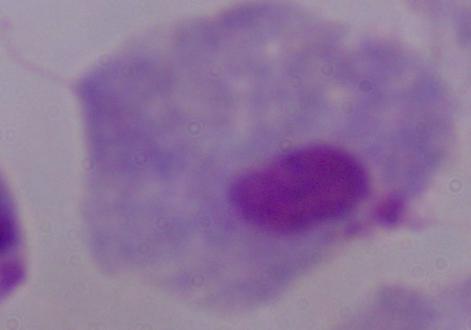
Captured at 1000x magnification. A trichomonad is seen. Micrograph.